Assess the morphology of the red blood cells.
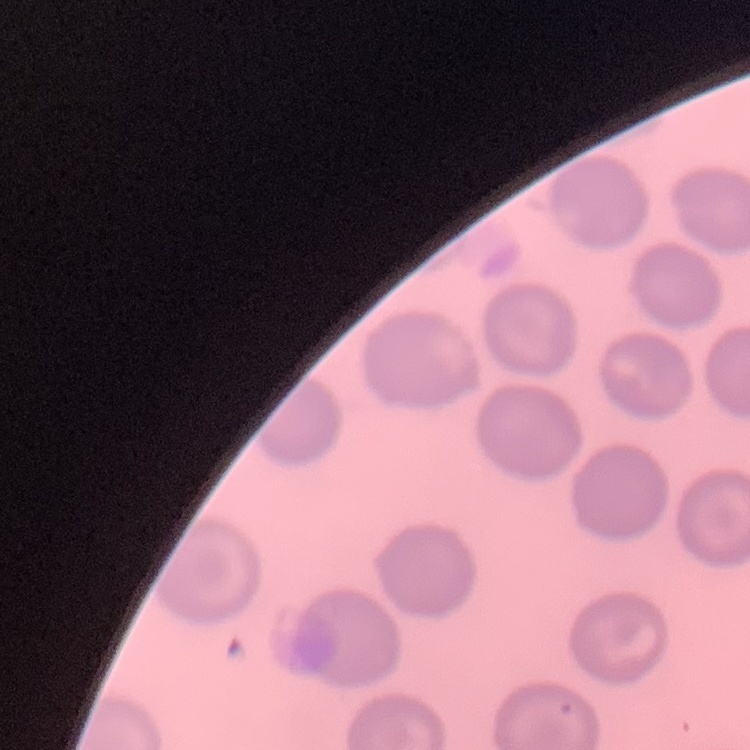
No rouleaux formation.

{
  "preparation": "thin blood film",
  "stain": "Field's or Giemsa",
  "image_type": "square crop of a larger photomicrograph"
}